Report the malaria status of this cell.
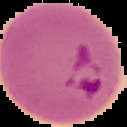
Parasitized.

From a thin blood smear. The area outside the segmented cell region is set to black. Image is 127×127 pixels.